State which parasite is depicted.
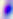

This is Toxoplasma gondii.

Summary:
  - Modality: photomicrograph
  - Magnification: 400x